Give the extent of all uninfected red blood cells.
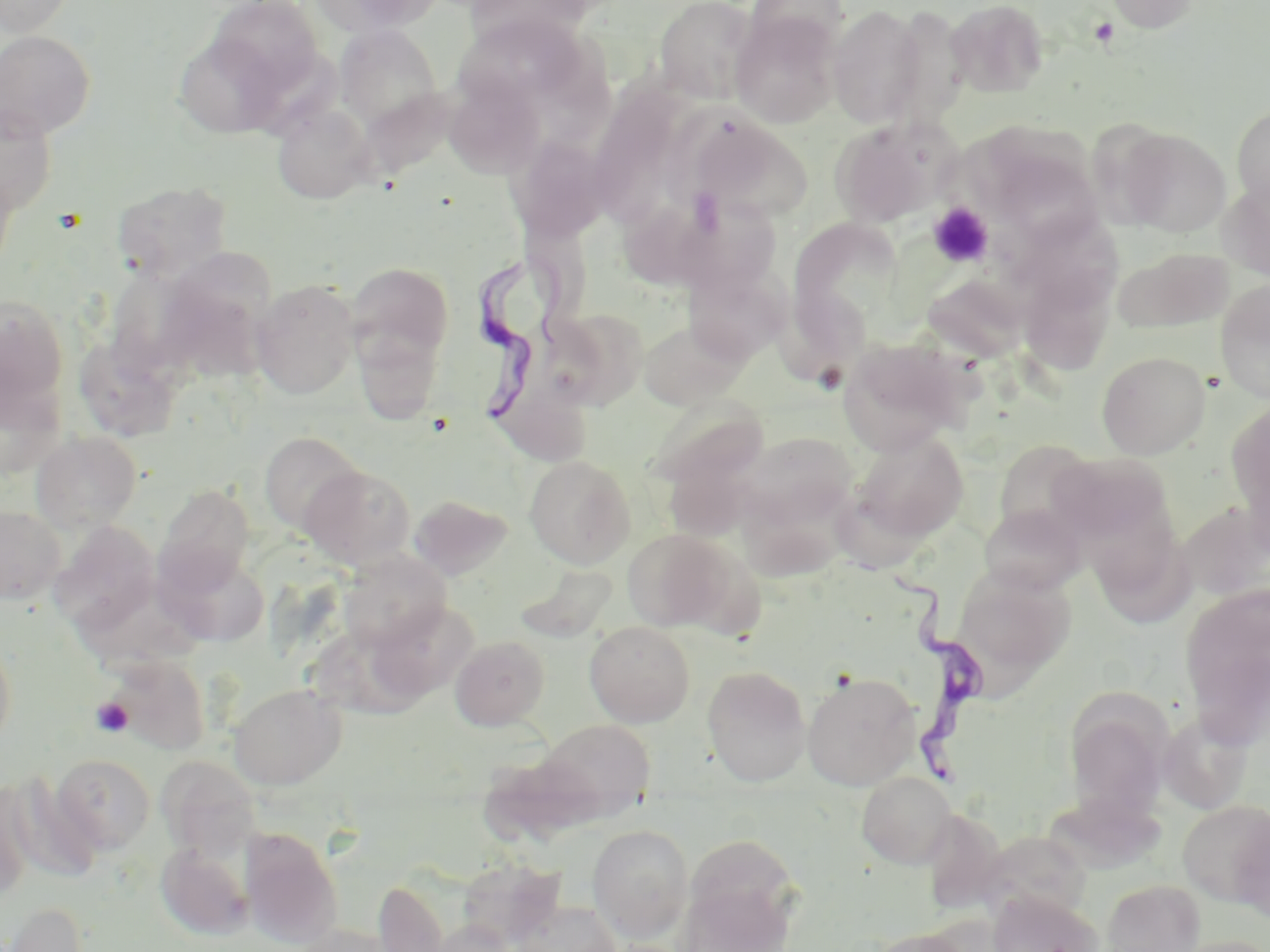

Approximate bounding boxes as [x1, y1, x2, y2] in pixels.
Uninfected red blood cells: [0, 0, 78, 36], [205, 0, 325, 102], [312, 0, 443, 36], [653, 0, 760, 103], [744, 0, 850, 58], [946, 0, 1049, 98], [1105, 0, 1200, 33], [460, 1, 599, 48], [828, 4, 927, 128], [731, 14, 840, 128], [334, 23, 443, 134], [452, 24, 589, 101], [0, 29, 96, 140], [173, 31, 289, 141], [442, 71, 548, 179], [601, 78, 690, 221], [0, 103, 57, 217], [272, 104, 377, 203], [1232, 104, 1270, 212], [688, 114, 809, 225], [829, 117, 959, 229], [1119, 128, 1231, 237], [506, 136, 611, 244], [988, 144, 1105, 249], [0, 158, 21, 280], [1219, 177, 1270, 279], [110, 179, 232, 283], [618, 193, 716, 290], [684, 199, 786, 293], [802, 222, 907, 352], [1013, 224, 1130, 327], [1114, 247, 1233, 334], [160, 255, 280, 362], [346, 261, 454, 371], [684, 263, 790, 365], [104, 267, 210, 378], [923, 275, 1031, 365], [251, 279, 360, 399], [1215, 280, 1270, 404], [1021, 287, 1122, 387], [0, 294, 70, 410], [542, 307, 651, 412], [638, 321, 747, 409], [358, 324, 449, 433], [76, 338, 181, 442], [838, 338, 966, 456], [1097, 351, 1210, 459], [0, 368, 64, 479], [647, 397, 768, 495], [1228, 400, 1270, 527], [30, 430, 143, 533], [853, 430, 969, 542], [259, 432, 364, 534], [741, 432, 858, 531], [991, 441, 1100, 544], [1046, 452, 1176, 557], [524, 456, 635, 568], [301, 464, 417, 569], [154, 484, 256, 595], [409, 494, 513, 580], [739, 500, 853, 582], [978, 502, 1085, 596], [1178, 502, 1270, 604], [0, 505, 66, 605], [50, 521, 160, 635], [1091, 523, 1195, 628], [622, 528, 734, 633], [690, 546, 781, 637], [161, 549, 271, 648], [339, 550, 451, 652], [952, 567, 1076, 687], [74, 577, 206, 666], [1180, 585, 1270, 734], [374, 600, 480, 700], [584, 621, 695, 726], [0, 627, 17, 755], [309, 631, 437, 722], [450, 635, 550, 731], [105, 655, 212, 755], [701, 665, 812, 787], [802, 671, 920, 790], [228, 684, 346, 790], [1065, 692, 1173, 820], [1157, 709, 1253, 815], [538, 719, 655, 818], [52, 755, 156, 854], [157, 756, 261, 859], [857, 770, 957, 868], [3, 774, 103, 884], [0, 782, 33, 902], [1178, 800, 1270, 907], [935, 809, 1005, 912], [1234, 811, 1270, 922], [588, 824, 693, 940], [240, 827, 343, 948], [973, 830, 1093, 923], [684, 834, 801, 942], [156, 842, 254, 940], [455, 857, 564, 950], [373, 876, 451, 952], [1100, 879, 1205, 952], [676, 883, 789, 951], [987, 891, 1102, 952], [511, 898, 622, 952], [1, 900, 91, 952], [429, 919, 516, 952], [293, 923, 398, 952], [866, 927, 974, 952], [1168, 935, 1270, 952].

Trypanosoma brucei locations: [474, 259, 593, 438], [887, 559, 990, 792]. Platelet locations: [1089, 17, 1119, 47], [927, 202, 994, 268], [91, 697, 133, 738]. Slide-level diagnosis: Trypanosoma brucei. Optical microscopy. May-Grünwald-Giemsa-stained preparation. 1000x magnification. Image is 1270×952 pixels. One field of a larger specimen. Thin blood smear.